Name the parasite shown.
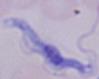

This is a trypanosome.

Captured at 1000x magnification. Micrograph.